State which parasite is depicted.
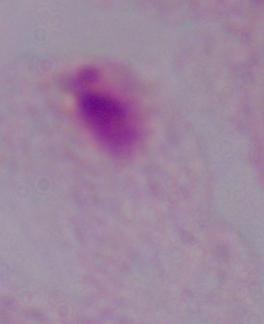
This is a trichomonad.

Captured at 1000x magnification. Micrograph.